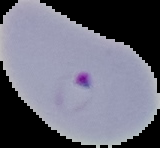

preparation = thin blood smear
image type = segmented cell region with the area outside set to black
result = malaria parasites identified
image size = 160×148 pixels